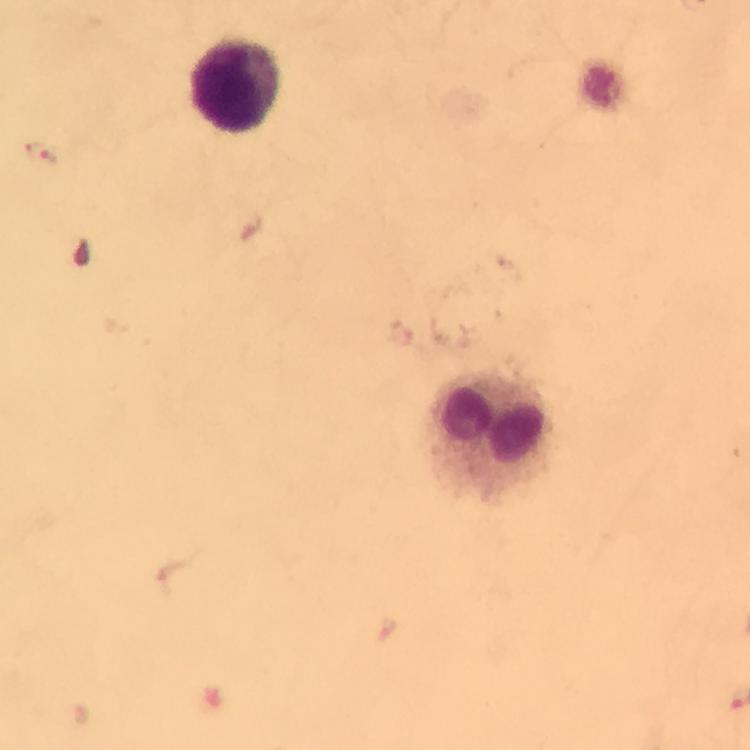 Approximate centers as [x, y] in pixels. Leukocyte locations: [236, 86], [489, 433]. Malaria parasite locations: [43, 152]. From a malaria diagnostic workup. A crop from one field of view. Photographed through the microscope with a smartphone camera. Giemsa stain. At 100x magnification. Immersion oil was used. Image is 750×750 pixels. Thick blood film.